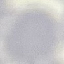 Result: no malaria parasites seen. Thin smear of blood. Cell patch, automatically extracted from a larger field of view and resized to 64 × 64 pixels. Acquired by smartphone through the microscope eyepiece. Giemsa-stained preparation.